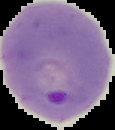

{
  "preparation": "thin blood smear",
  "image_type": "segmented cell region with the area outside set to black",
  "malaria_status": "parasitized",
  "image_size": "115×130 pixels"
}